State the blood parasite species.
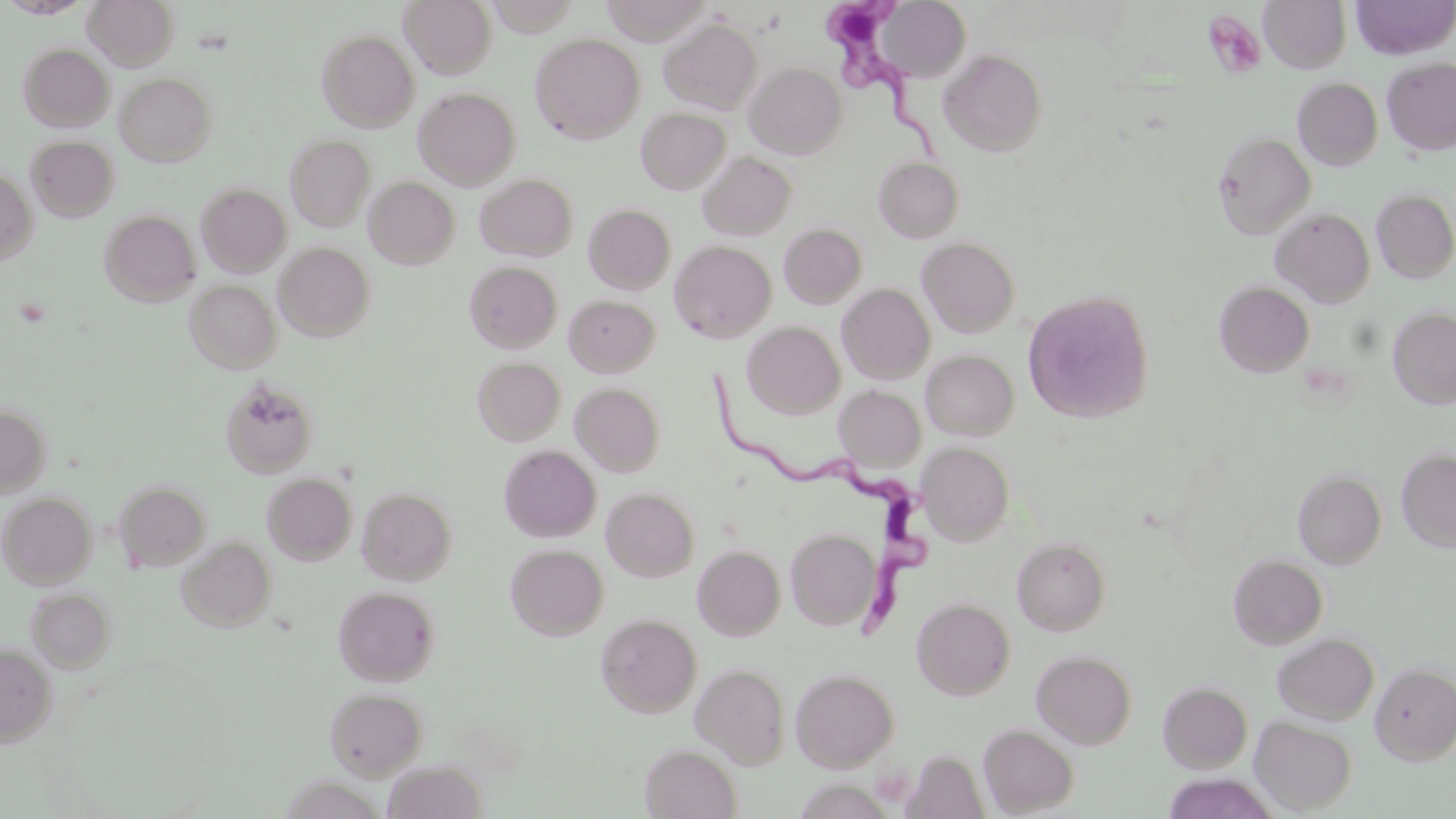

Trypanosoma brucei.

Summary:
  - Coordinate format: approximate bounding boxes as (x1, y1, x2, y2) in pixels
  - Trypanosoma brucei locations: (827, 0, 957, 171), (709, 366, 934, 636)
  - Uninfected red blood cell locations: (85, 0, 178, 70), (400, 0, 496, 78), (1260, 0, 1351, 73), (1351, 0, 1455, 59), (878, 1, 971, 81), (661, 17, 762, 115), (316, 28, 419, 132), (531, 32, 645, 144), (19, 43, 114, 132), (939, 48, 1047, 156), (1382, 57, 1456, 155), (745, 62, 846, 158), (116, 72, 216, 166), (1294, 77, 1383, 170), (414, 87, 520, 189), (636, 106, 729, 194), (1214, 130, 1316, 239), (285, 134, 376, 231), (26, 136, 119, 222), (698, 152, 798, 240), (874, 157, 963, 242), (0, 170, 37, 265), (475, 173, 578, 261), (364, 176, 460, 269), (196, 183, 292, 276), (1371, 188, 1456, 283), (584, 203, 675, 295), (1271, 207, 1375, 307), (100, 209, 201, 306), (779, 223, 867, 309), (917, 236, 1021, 338), (669, 240, 776, 342), (275, 242, 376, 341), (464, 261, 562, 352), (186, 280, 281, 373), (1214, 280, 1315, 377), (837, 283, 936, 384), (1022, 289, 1155, 423), (564, 294, 660, 377), (1388, 306, 1456, 409), (742, 321, 845, 418), (922, 349, 1019, 440), (473, 357, 565, 445), (220, 378, 318, 478), (571, 382, 665, 476), (834, 385, 926, 472), (0, 403, 51, 496), (917, 442, 1014, 544), (498, 444, 601, 542), (1397, 448, 1456, 552), (1293, 469, 1386, 569), (262, 472, 357, 565), (115, 480, 212, 570), (357, 486, 457, 585), (602, 487, 699, 581), (0, 491, 97, 588), (786, 528, 881, 629), (177, 536, 276, 632), (1012, 537, 1110, 635), (506, 544, 608, 640), (693, 544, 786, 640), (1228, 553, 1328, 649), (333, 585, 439, 685), (28, 587, 115, 671), (911, 597, 1015, 699), (595, 613, 701, 719), (1273, 633, 1379, 725), (0, 644, 57, 748), (1032, 650, 1137, 749), (691, 662, 790, 768), (1370, 662, 1456, 763), (791, 668, 899, 772), (1159, 681, 1253, 773), (325, 686, 427, 779), (1251, 716, 1357, 814), (979, 725, 1079, 816), (641, 744, 741, 819), (384, 760, 486, 819), (1160, 774, 1280, 819)
  - Platelet locations: (1202, 10, 1267, 78)
  - Magnification: 1000x
  - Image size: 1456×819 pixels
  - Stain: May-Grünwald-Giemsa
  - Field of view: single
  - Modality: light microscopy
  - Preparation: thin blood film